State which cell type is depicted.
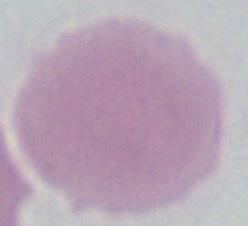

An erythrocyte.

magnification: 1000x
modality: micrograph